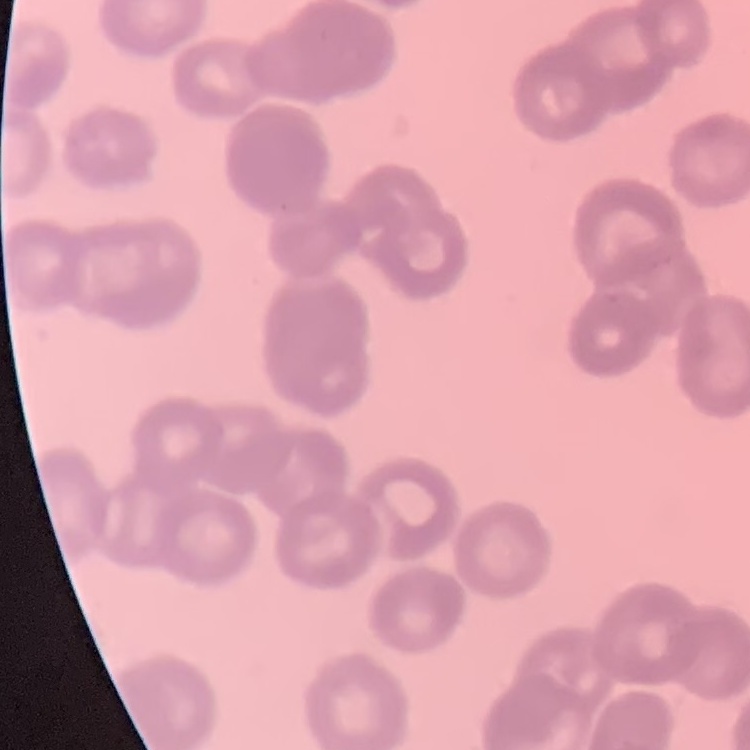
Summary:
  - Erythrocyte morphology: rouleaux formation
  - Image type: square crop of a larger photomicrograph
  - Preparation: thin peripheral smear
  - Stain: Field's or Giemsa